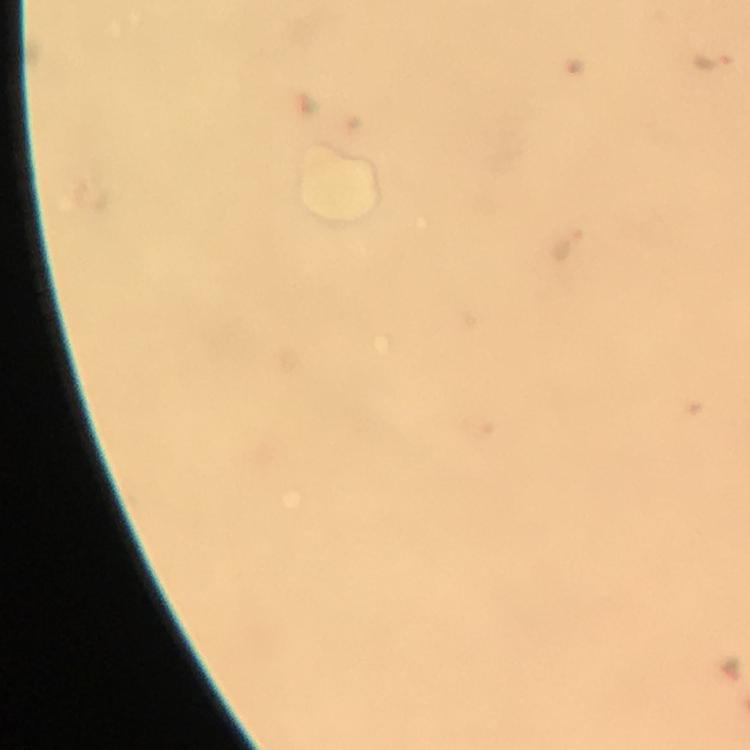 Approximate object centers, in pixels from the top-left corner. Plasmodium parasite locations: (x=714, y=61), (x=565, y=245). Immersion oil was used. Smartphone photograph taken through a microscope. Thick blood smear. Image is 750×750 pixels. 100x magnification. Giemsa stain. Cropped region of a single field of view. From a malaria diagnostic workup.